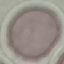
Summary:
  - Malaria status: uninfected
  - Capture: smartphone through the microscope eyepiece
  - Preparation: thin smear
  - Image type: automatically extracted cell patch, resized to 64 × 64 pixels
  - Stain: Giemsa